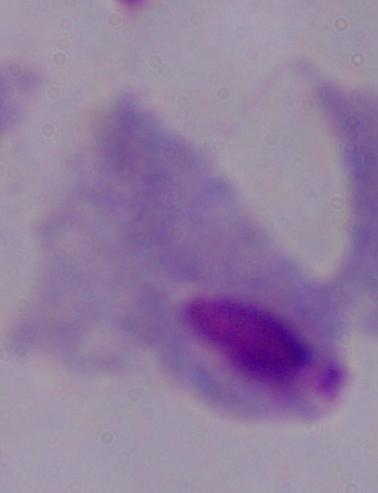

modality = photomicrograph
identification = trichomonad
magnification = 1000x